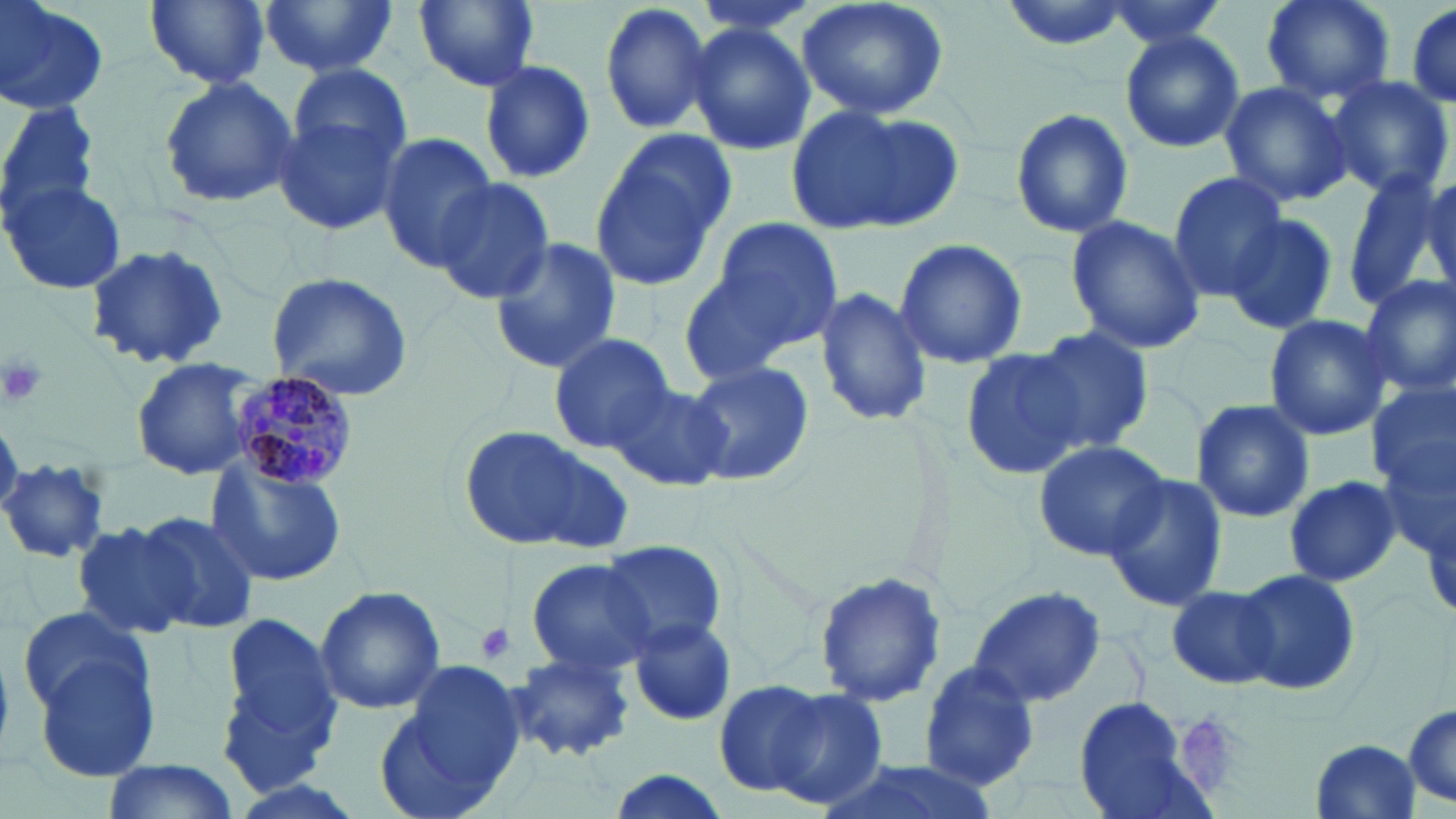

slide-level diagnosis = Plasmodium malariae
preparation = thin blood film
uninfected red blood cell locations = approximate bounding boxes as (x1,y1)-(x2,y2) corner pairs in pixels: (0,0)-(107,116), (146,0)-(269,89), (260,0)-(400,77), (409,0)-(543,94), (597,0)-(717,137), (688,0)-(823,37), (797,0)-(950,122), (996,0)-(1139,50), (1098,0)-(1237,48), (1261,0)-(1394,104), (1403,1)-(1456,112), (686,20)-(815,158), (1120,29)-(1246,155), (292,61)-(413,166), (479,62)-(595,182), (1323,75)-(1454,199), (156,76)-(300,211), (1219,82)-(1355,209), (272,93)-(409,240), (0,101)-(101,219), (786,102)-(956,238), (1011,107)-(1134,238), (376,132)-(498,269), (589,133)-(735,291), (1167,171)-(1288,300), (1344,173)-(1447,314), (1418,174)-(1456,302), (432,177)-(555,304), (4,180)-(127,296), (1227,213)-(1339,336), (696,215)-(844,363), (1063,215)-(1209,357), (487,236)-(622,376), (893,237)-(1028,368), (82,244)-(229,371), (263,270)-(413,401), (1358,274)-(1456,399), (814,285)-(933,429), (1263,313)-(1393,441), (1028,325)-(1156,455), (547,332)-(677,454), (960,344)-(1089,480), (130,356)-(267,481), (685,359)-(813,488), (605,380)-(732,492), (1367,381)-(1455,505), (1190,397)-(1315,524), (1376,415)-(1456,571), (455,424)-(628,553), (1032,438)-(1171,562), (207,454)-(346,588), (0,457)-(112,565), (1102,472)-(1230,609), (1282,476)-(1399,586), (129,510)-(260,633), (70,521)-(204,639), (595,539)-(729,653), (525,557)-(660,678), (1236,567)-(1361,696), (813,570)-(949,706), (315,585)-(445,716), (967,585)-(1106,708), (1167,585)-(1277,690), (16,608)-(149,717), (215,611)-(343,792), (629,622)-(739,727), (32,643)-(165,787), (508,653)-(633,762), (379,656)-(525,818), (918,661)-(1042,790), (726,680)-(891,811), (1074,696)-(1211,819), (1402,703)-(1456,810), (1308,736)-(1421,819), (811,756)-(995,819), (100,760)-(241,819), (600,769)-(735,819)
Plasmodium malariae-infected red blood cell locations = approximate bounding boxes as (x1,y1)-(x2,y2) corner pairs in pixels: (226,373)-(360,490)
modality = optical microscopy
image size = 1456×819 pixels
field of view = one of a larger specimen
stain = May-Grünwald-Giemsa
magnification = 1000x
platelet locations = approximate bounding boxes as (x1,y1)-(x2,y2) corner pairs in pixels: (0,353)-(48,409), (474,623)-(515,665), (1185,717)-(1237,791)